Comment on the morphology of the erythrocytes.
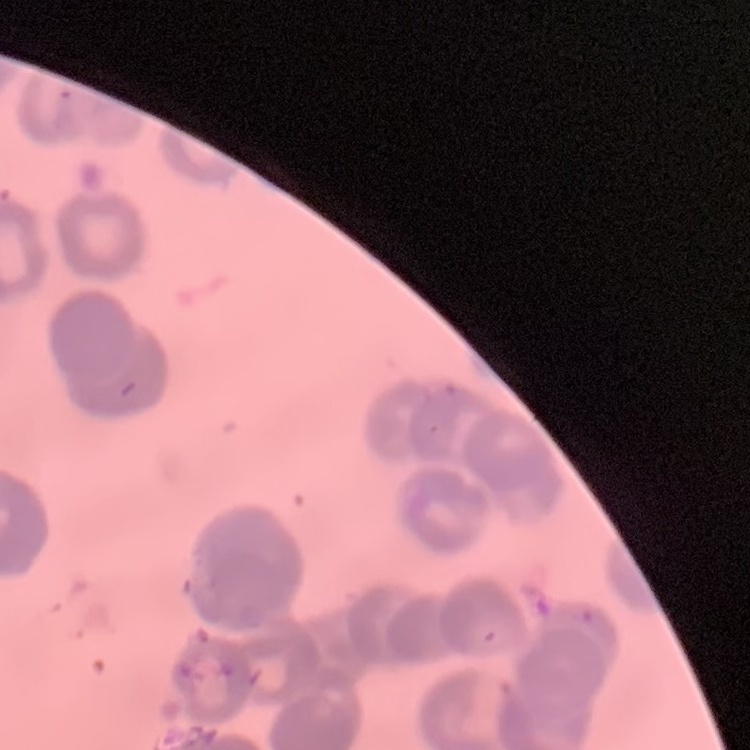
Rouleaux formation.

Summary:
  - Preparation: thin peripheral smear
  - Stain: Field's or Giemsa
  - Image type: square crop of a larger photomicrograph